Assess the morphology of the erythrocytes.
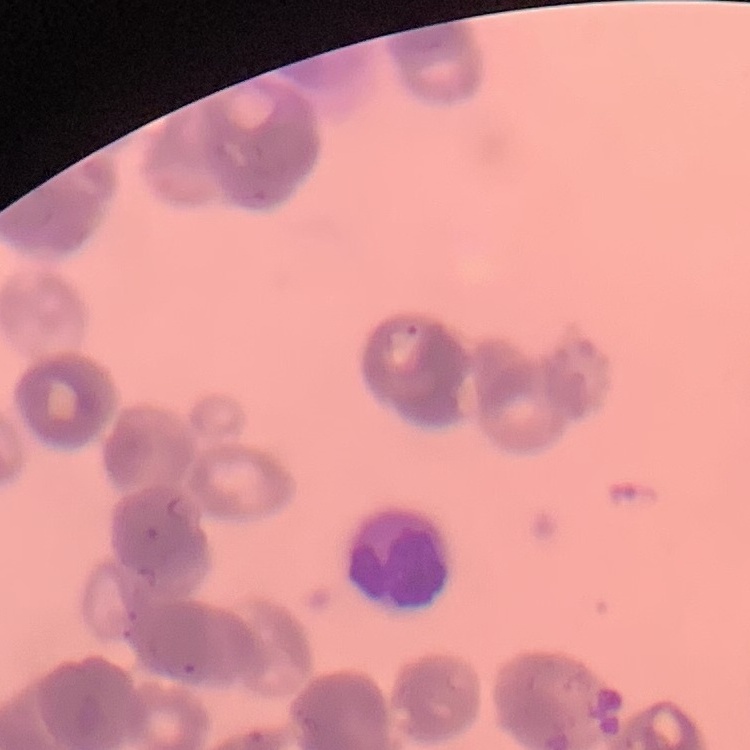

They show rouleaux formation.

One tile cut from a larger photomicrograph. Thin blood smear. Stained with either Field's or Giemsa.